Point out each Plasmodium parasite.
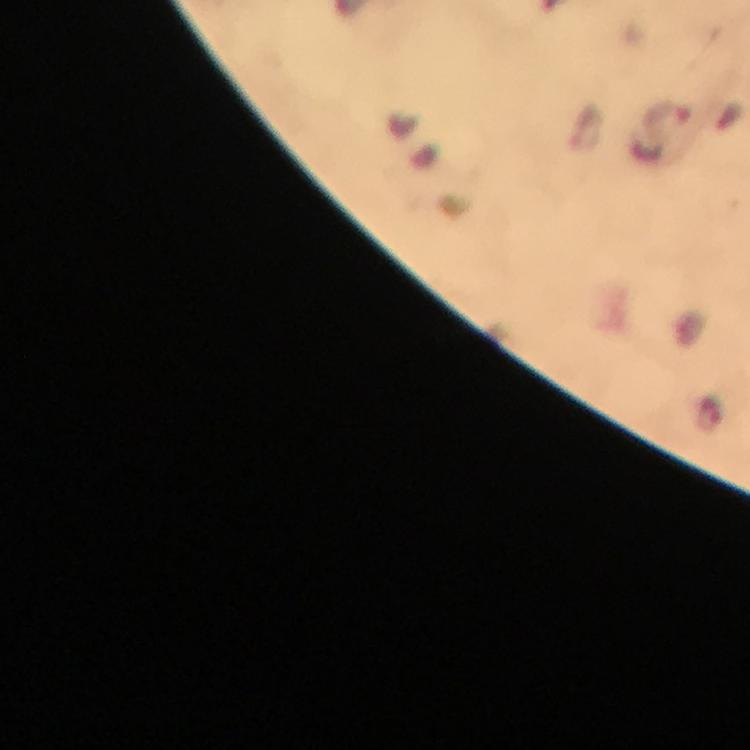

Approximate object centers, in pixels from the top-left corner.
Plasmodium parasites: (x=668, y=116), (x=711, y=413).

Summary:
  - Magnification: 100x
  - Preparation: thick smear
  - Cropped from: a single field of view
  - Immersion oil: applied
  - Context: from a diagnostic examination for malaria
  - Stain: Giemsa
  - Image size: 750×750 pixels
  - Capture: smartphone mounted on the microscope